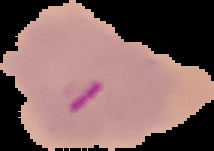

{
  "image_type": "cell region segmented out of the field of view; surrounding area masked to black",
  "image_size": "214×151 pixels",
  "preparation": "thin blood film",
  "malaria_status": "parasitized"
}